Describe the morphology of the red blood cells.
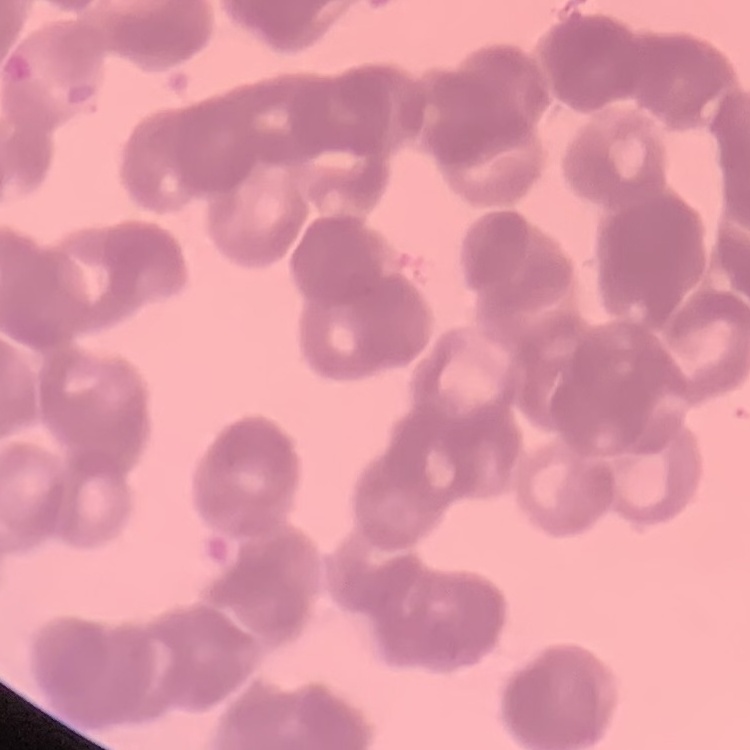

Rouleaux formation.

Summary:
  - Stain: Field's or Giemsa
  - Preparation: thin peripheral smear
  - Image type: one tile cut from a larger photomicrograph